Point out each leukocyte.
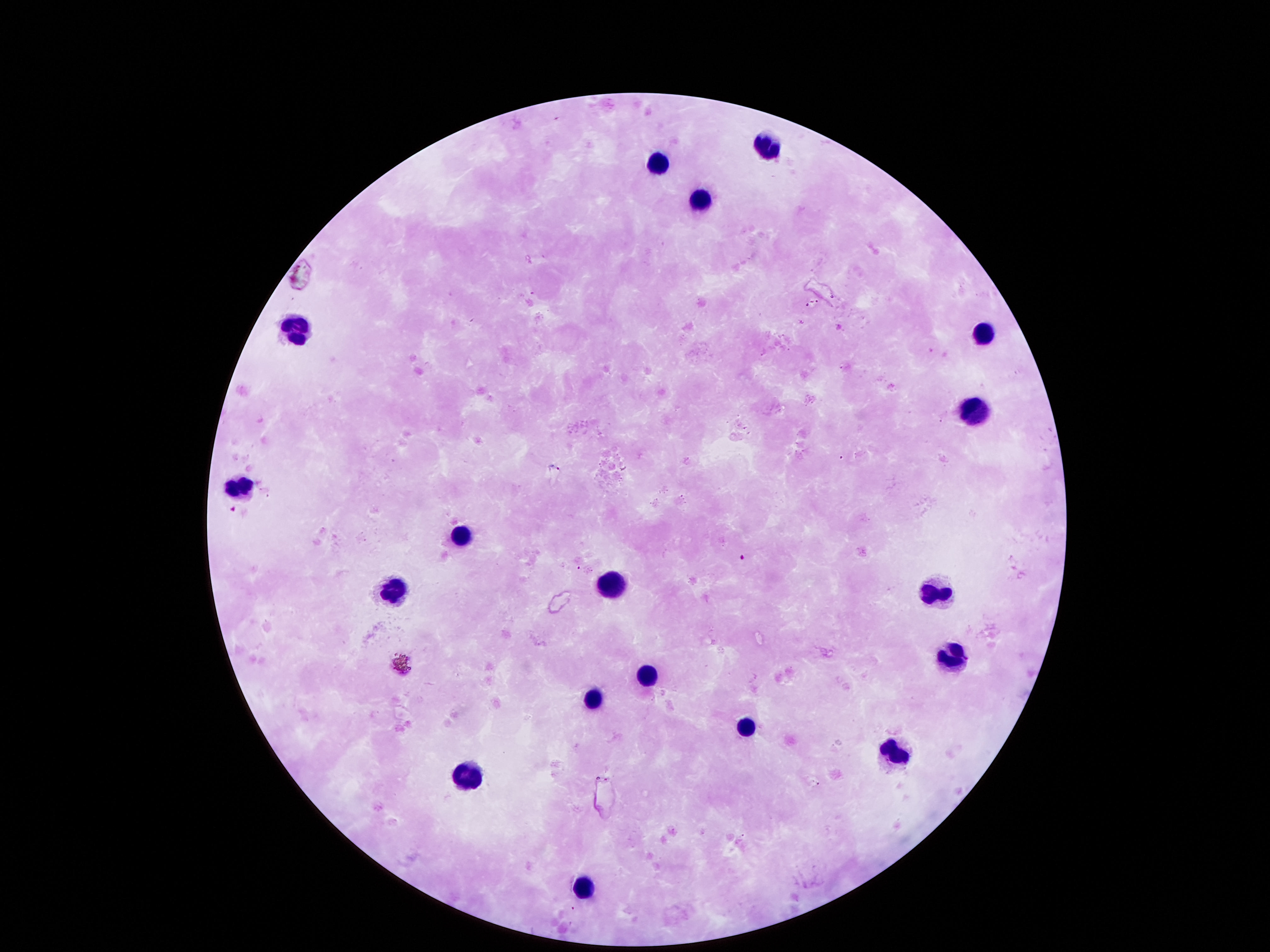

Approximate centers as [x, y] in pixels.
Leukocytes: [769, 142], [657, 162], [704, 196], [299, 330], [981, 336], [975, 408], [234, 491], [458, 537], [610, 582], [934, 591], [392, 593], [953, 653], [642, 672], [595, 693], [744, 724], [891, 750], [470, 775], [582, 881].

Photographed through the microscope eyepiece with a smartphone camera. Giemsa-stained preparation. Patient malaria status: negative. Thick blood film. Image is 1270×952 pixels. 100x magnification. Single field of view.